Assess the morphology of the red blood cells.
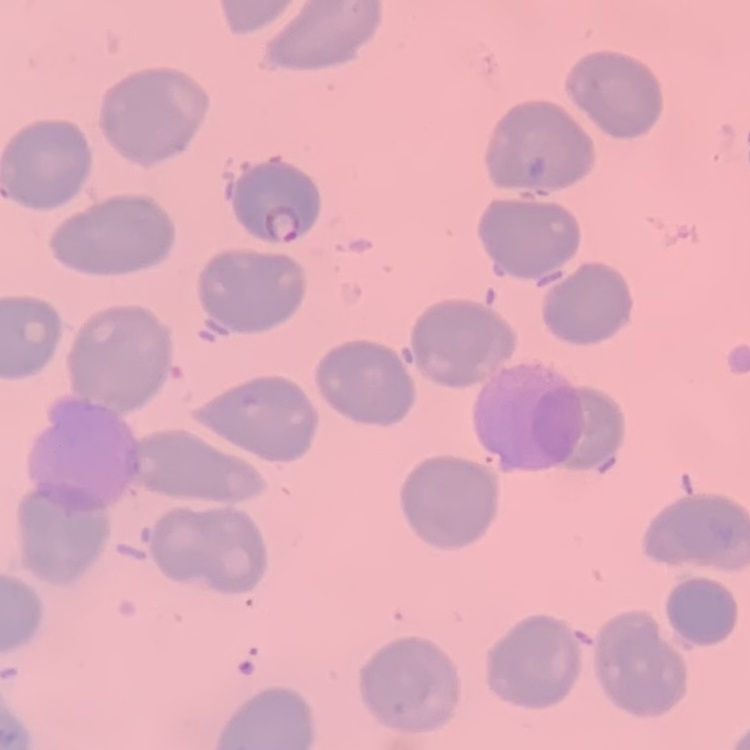
They show no rouleaux formation.

stain: Field's or Giemsa
preparation: thin peripheral smear
image_type: square crop of a larger photomicrograph